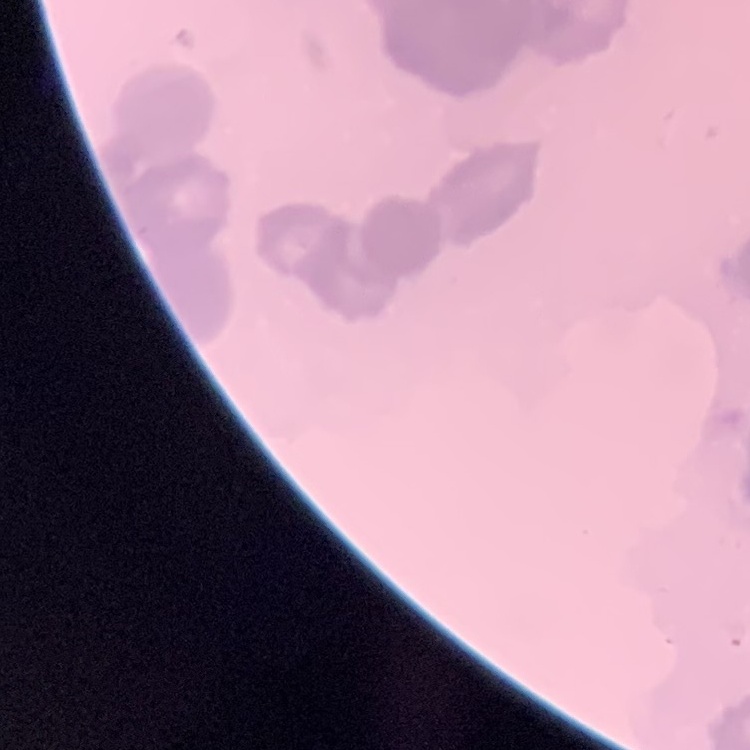

The red blood cells show rouleaux formation. Square crop of a larger photomicrograph. Stained with either Field's or Giemsa. Thin blood smear.